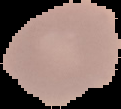

Summary:
  - Preparation: thin blood smear
  - Image size: 121×109 pixels
  - Result: no malaria parasites detected
  - Image type: segmented cell region with the area outside set to black